Classify this cell by malaria status.
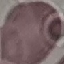

It is uninfected.

Summary:
  - Stain: Giemsa
  - Image type: cell patch, automatically extracted from a larger field of view and resized to 64 × 64 pixels
  - Preparation: thin smear
  - Capture: smartphone through the microscope eyepiece